Comment on the morphology of the erythrocytes.
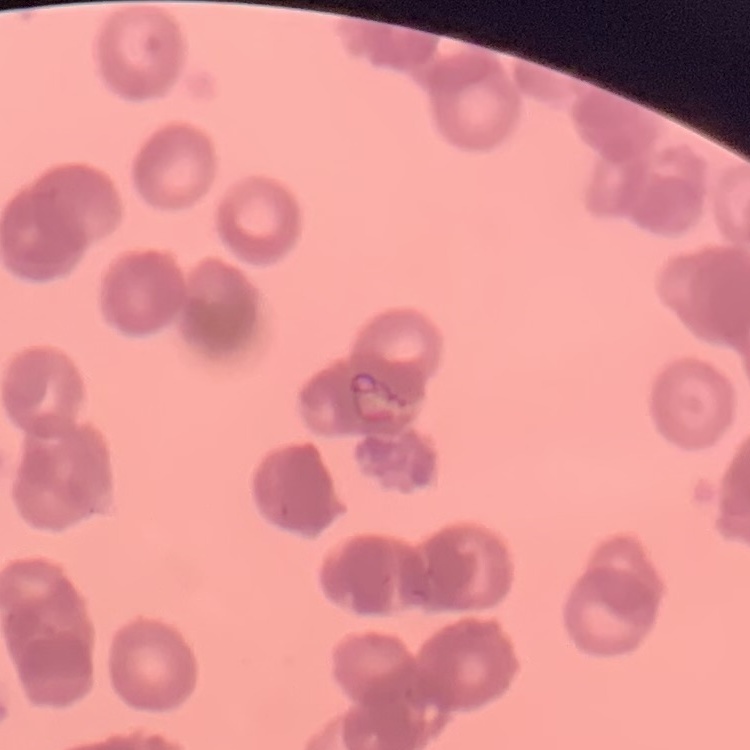
They show rouleaux formation.

stain: Field's or Giemsa
image_type: one tile cut from a larger photomicrograph
preparation: thin peripheral smear